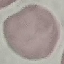 Result: no malaria parasites detected. Giemsa stain. Acquired by smartphone through the microscope eyepiece. Thin blood smear. Automatically extracted cell patch, resized to 64 × 64 pixels.